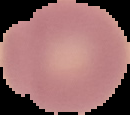
image size = 130×115 pixels
preparation = thin blood smear
malaria status = uninfected
image type = segmented cell region on a black background